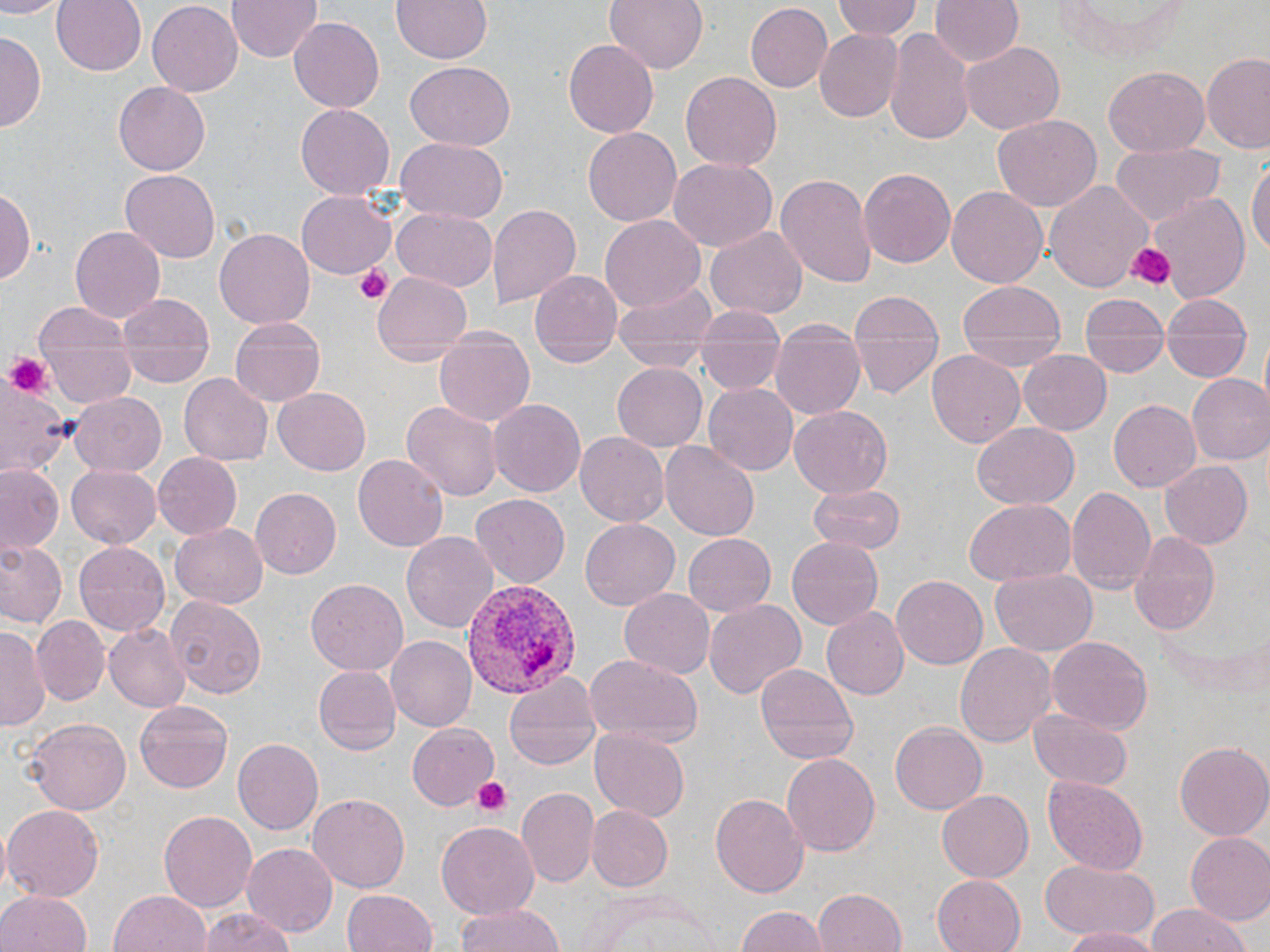
slide-level diagnosis = Plasmodium vivax
magnification = 1000x
modality = optical microscopy
platelet locations = approximate bounding boxes as (x1, y1, x2, y2) in pixels: (1126, 242, 1174, 290), (353, 264, 394, 305), (3, 353, 53, 398), (469, 776, 516, 818)
field of view = single
preparation = thin blood smear
uninfected red blood cell locations = approximate bounding boxes as (x1, y1, x2, y2) in pixels: (0, 0, 61, 18), (51, 0, 147, 77), (228, 0, 320, 62), (387, 0, 495, 65), (604, 0, 706, 76), (835, 0, 922, 42), (929, 0, 1023, 69), (1054, 0, 1194, 65), (147, 1, 243, 94), (559, 3, 707, 128), (744, 3, 832, 92), (942, 7, 1049, 110), (289, 17, 385, 112), (814, 26, 905, 122), (884, 26, 977, 149), (0, 34, 44, 131), (564, 40, 657, 138), (957, 41, 1063, 135), (1202, 52, 1270, 154), (406, 63, 515, 149), (1104, 68, 1207, 155), (679, 73, 782, 171), (113, 83, 210, 175), (294, 105, 394, 198), (993, 114, 1102, 211), (582, 128, 682, 226), (396, 138, 509, 222), (1109, 141, 1221, 225), (668, 155, 775, 249), (1248, 157, 1270, 260), (859, 167, 956, 267), (120, 169, 217, 262), (774, 171, 878, 289), (1046, 179, 1153, 291), (3, 182, 36, 290), (946, 186, 1046, 289), (297, 190, 394, 277), (1147, 192, 1250, 305), (485, 201, 581, 308), (391, 206, 497, 291), (599, 216, 705, 313), (70, 224, 165, 321), (705, 224, 808, 317), (214, 229, 313, 330), (371, 268, 473, 363), (529, 268, 623, 365), (613, 277, 716, 368), (955, 283, 1067, 375), (120, 288, 217, 377), (844, 288, 946, 401), (1078, 301, 1168, 378), (33, 302, 133, 356), (229, 316, 327, 407), (769, 323, 865, 422), (433, 328, 534, 428), (1161, 330, 1253, 378), (695, 333, 781, 392), (41, 343, 135, 407), (927, 350, 1025, 449), (1017, 350, 1112, 436), (702, 351, 782, 426), (611, 361, 707, 450), (179, 373, 273, 468), (1187, 373, 1270, 467), (1, 378, 71, 481), (704, 382, 797, 474), (273, 388, 371, 475), (67, 393, 167, 477), (402, 398, 501, 504), (487, 398, 586, 498), (1108, 399, 1201, 492), (790, 406, 893, 496), (972, 421, 1079, 510), (575, 432, 669, 525), (661, 440, 759, 541), (153, 453, 241, 539), (355, 453, 447, 553), (1158, 459, 1255, 550), (1, 464, 63, 554), (65, 464, 162, 549), (1065, 483, 1158, 596), (806, 484, 907, 552), (249, 487, 340, 579), (471, 494, 569, 587), (965, 499, 1076, 585), (578, 519, 678, 609), (169, 522, 268, 608), (403, 530, 499, 638), (1130, 530, 1222, 634), (684, 533, 776, 617), (786, 535, 884, 631), (0, 538, 66, 630), (72, 539, 170, 634), (991, 569, 1098, 656), (892, 574, 988, 669), (306, 577, 407, 675), (618, 587, 714, 680), (167, 596, 267, 699), (703, 599, 806, 700), (823, 608, 908, 698), (32, 614, 110, 707), (106, 621, 190, 713), (1, 626, 44, 731), (387, 637, 476, 731), (1047, 637, 1152, 733), (956, 641, 1056, 747), (583, 651, 704, 750), (754, 663, 859, 765), (312, 665, 401, 753), (502, 673, 601, 774), (134, 701, 232, 793), (1028, 707, 1134, 789), (27, 716, 132, 815), (890, 722, 987, 813), (409, 724, 499, 808), (589, 728, 690, 823), (232, 740, 323, 837), (1175, 741, 1270, 842), (782, 753, 881, 857), (1043, 776, 1150, 875), (520, 786, 599, 888), (937, 788, 1034, 883), (308, 792, 409, 891), (710, 792, 809, 898), (4, 803, 104, 901), (585, 804, 672, 892), (159, 810, 256, 911), (435, 821, 539, 921), (1184, 833, 1270, 926), (242, 842, 337, 938), (1041, 860, 1158, 942), (931, 874, 1024, 952), (814, 887, 909, 952), (341, 888, 438, 952), (0, 889, 91, 952), (108, 889, 212, 952), (580, 890, 722, 952), (455, 903, 567, 952), (1145, 905, 1249, 952), (732, 906, 829, 952), (199, 909, 293, 952), (1061, 925, 1159, 952)
image size = 1270×952 pixels
Plasmodium vivax-infected red blood cell locations = approximate bounding boxes as (x1, y1, x2, y2) in pixels: (456, 576, 583, 700)
stain = May-Grünwald-Giemsa